Report the malaria status of this cell.
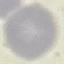
Uninfected.

{
  "preparation": "thin smear",
  "stain": "Giemsa",
  "image_type": "automatically extracted cell patch, resized to 64 × 64 pixels",
  "capture": "smartphone through the microscope eyepiece"
}